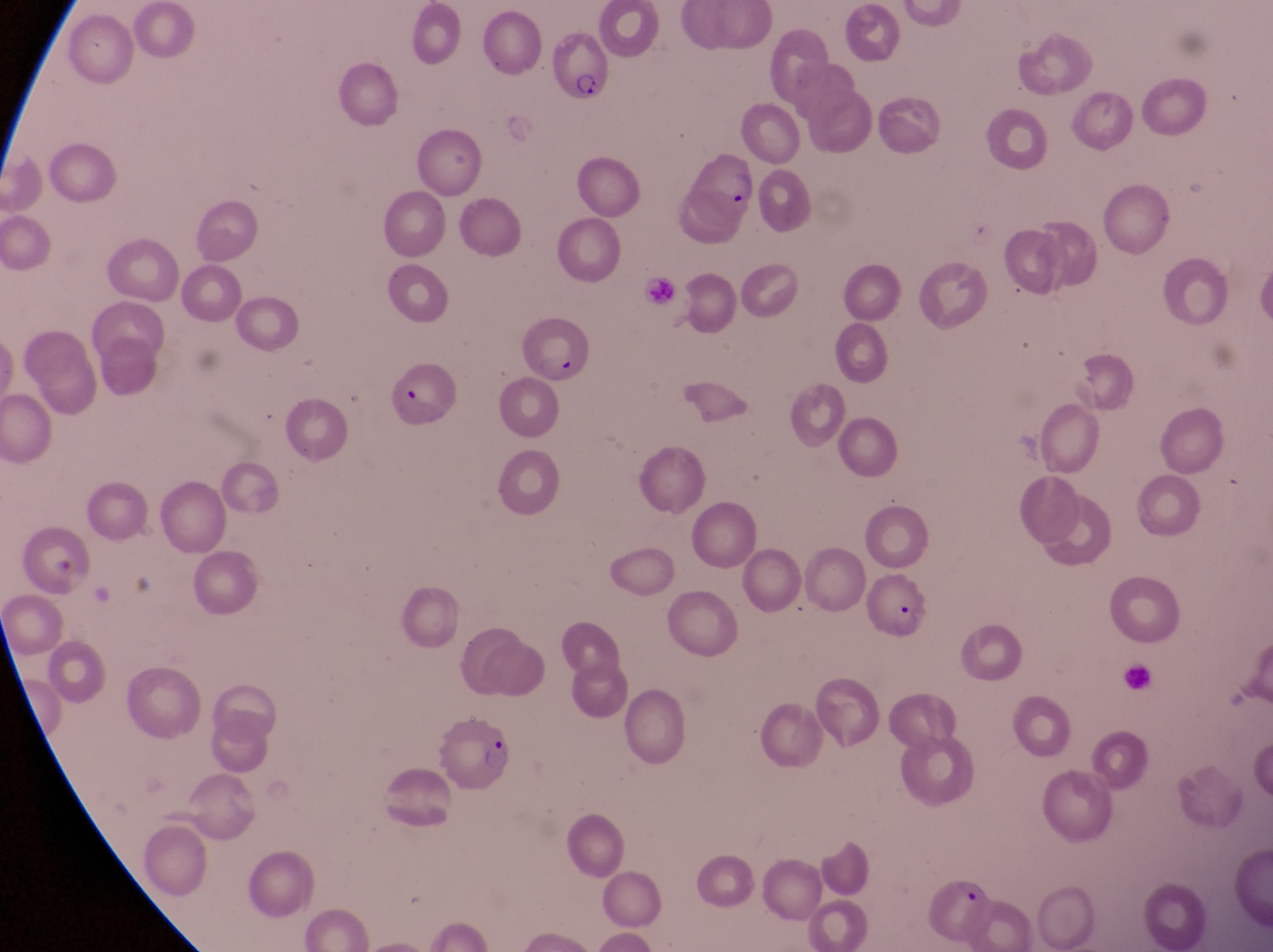

Approximate bounding boxes as [left, top, right, bottom] in pixels.
Summary:
  - Parasitised red blood cell locations: [547, 30, 612, 102], [681, 150, 766, 235], [517, 312, 597, 386], [385, 364, 454, 427], [864, 572, 933, 646], [430, 707, 515, 797], [928, 879, 995, 941]
  - Country: Uganda
  - Field of view: single
  - Preparation: thin blood film
  - Capture: smartphone photograph through the eyepiece of an Olympus CX-23 microscope
  - Image size: 1273×952 pixels
  - Magnification: 1000x